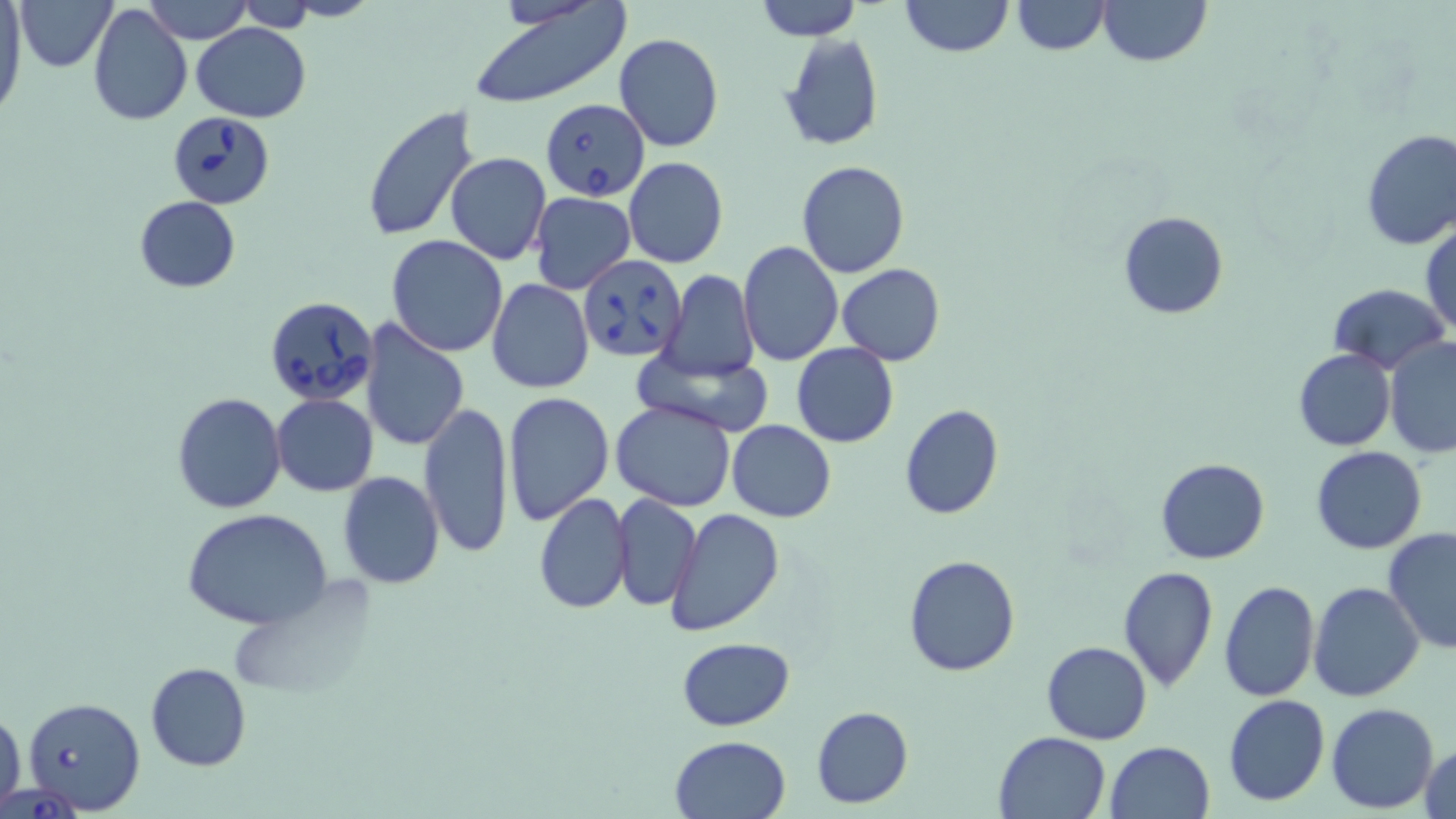
Summary:
  - Coordinate format: approximate bounding boxes as (x1,y1)-(x2,y2) corner pairs in pixels
  - Babesia divergens-infected red blood cell locations: (542,98)-(648,201), (159,108)-(278,219), (578,254)-(687,363), (264,296)-(378,406), (21,696)-(146,815), (2,783)-(89,817)
  - Uninfected red blood cell locations: (18,0)-(116,73), (144,0)-(250,44), (755,0)-(863,41), (899,0)-(1013,58), (1011,0)-(1108,55), (1098,0)-(1211,67), (235,1)-(317,30), (0,3)-(24,118), (88,4)-(192,127), (466,4)-(633,110), (190,22)-(310,122), (614,32)-(724,152), (779,32)-(884,153), (360,105)-(481,243), (1358,129)-(1456,250), (444,151)-(551,265), (624,156)-(728,268), (796,161)-(910,278), (530,192)-(636,293), (134,194)-(240,291), (1118,211)-(1229,319), (1420,218)-(1455,339), (386,235)-(508,356), (738,241)-(843,368), (836,263)-(945,365), (660,269)-(758,381), (486,279)-(594,395), (1327,283)-(1449,374), (358,318)-(469,450), (1384,336)-(1456,458), (791,344)-(898,448), (631,348)-(774,434), (1292,349)-(1397,451), (173,392)-(286,512), (502,392)-(614,525), (271,394)-(378,495), (611,399)-(739,511), (419,400)-(514,559), (617,403)-(729,627), (898,404)-(1004,520), (726,420)-(837,521), (1309,445)-(1428,555), (1155,458)-(1270,564), (337,470)-(445,589), (533,493)-(633,615), (613,493)-(701,611), (664,506)-(785,635), (181,507)-(334,629), (1382,527)-(1456,654), (903,555)-(1020,676), (1119,565)-(1219,692), (1218,579)-(1320,701), (1308,581)-(1425,701), (675,638)-(795,732), (1042,641)-(1151,745), (144,662)-(253,772), (1224,695)-(1330,806), (1326,702)-(1440,814), (811,704)-(912,808), (0,707)-(25,812), (993,732)-(1112,819), (668,734)-(792,819), (1105,741)-(1214,819), (1419,742)-(1455,819)
  - Slide-level diagnosis: Babesia divergens
  - Preparation: thin blood smear
  - Stain: May-Grünwald-Giemsa
  - Image size: 1456×819 pixels
  - Field of view: one of a larger specimen
  - Magnification: 1000x
  - Modality: optical microscopy